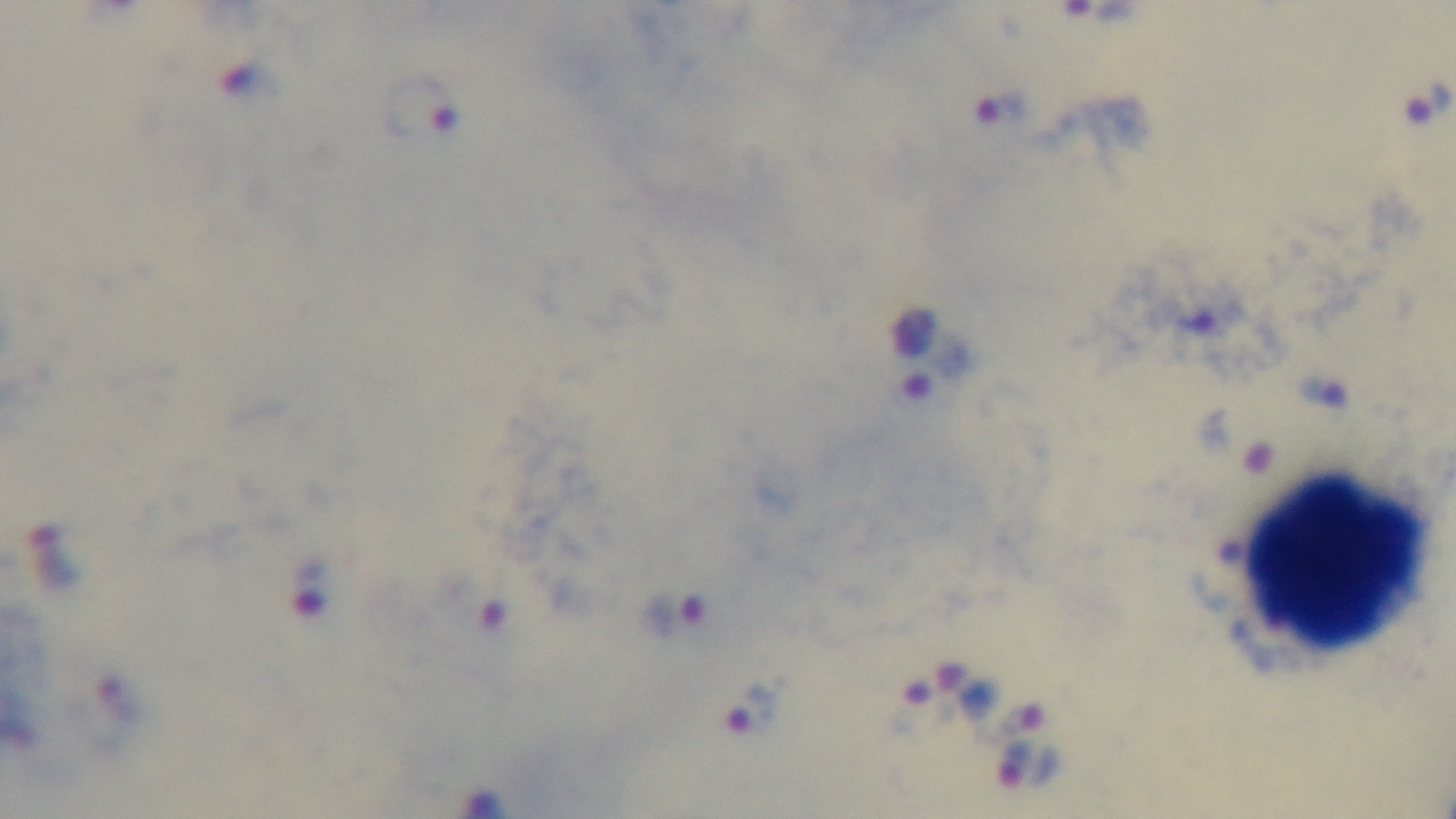
Summary:
  - Malaria status: infected
  - Capture: mounted 4K digital camera
  - Modality: light microscopy
  - Field of view: one from the slide
  - Objective: 100x oil immersion
  - Stain: Giemsa
  - Preparation: thick